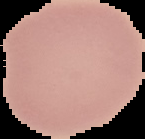 From a thin blood smear. The area outside the segmented cell region is set to black. Image is 145×139 pixels. Result: no Plasmodium parasites detected.